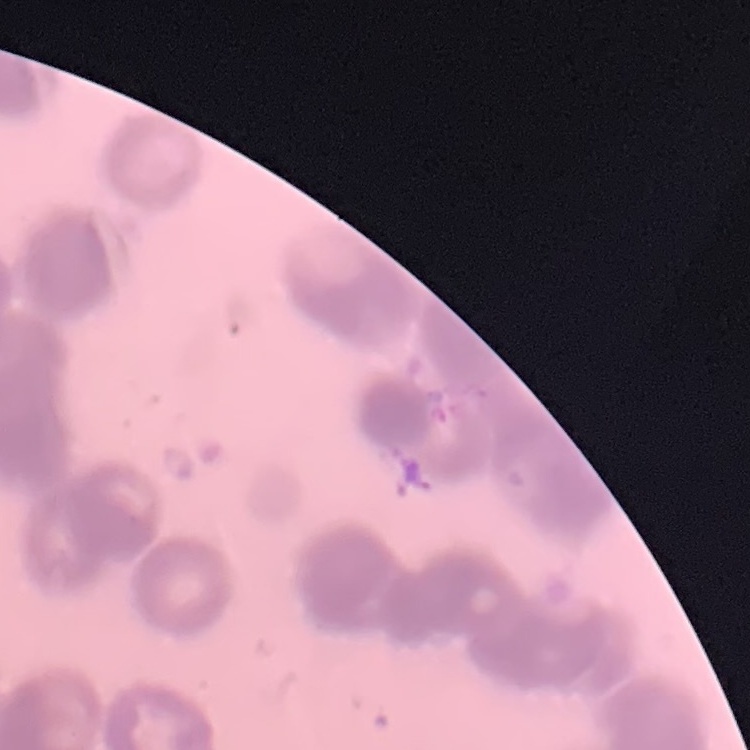 The red blood cells show rouleaux formation. Thin blood smear. One tile cut from a larger photomicrograph. Field's or Giemsa stain.